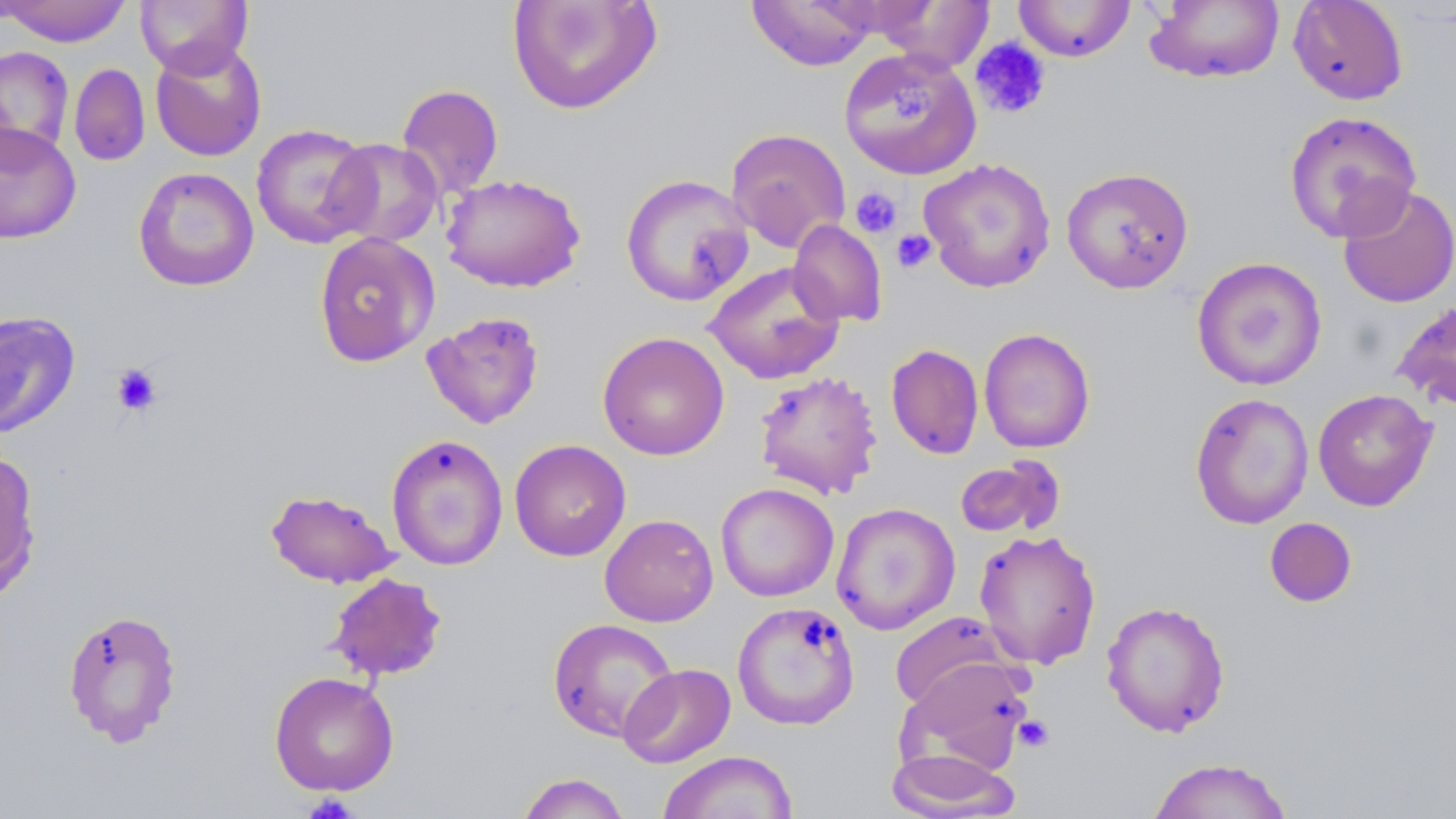

Approximate bounding boxes as [x1, y1, x2, y2] in pixels. Uninfected red blood cell locations: [2, 0, 133, 47], [135, 0, 252, 76], [507, 0, 661, 115], [747, 0, 880, 71], [875, 0, 994, 72], [1013, 0, 1135, 62], [1145, 0, 1285, 84], [1288, 0, 1409, 105], [150, 39, 267, 162], [0, 46, 74, 162], [839, 47, 982, 180], [69, 63, 150, 166], [397, 84, 504, 201], [1283, 110, 1423, 243], [0, 121, 82, 244], [250, 123, 377, 249], [725, 127, 851, 252], [324, 138, 444, 248], [918, 157, 1057, 293], [133, 166, 259, 292], [1061, 166, 1194, 293], [441, 173, 586, 293], [620, 173, 755, 307], [1337, 184, 1456, 309], [788, 219, 887, 327], [313, 232, 440, 368], [1191, 256, 1328, 391], [704, 260, 845, 385], [1391, 298, 1456, 411], [0, 311, 81, 439], [421, 311, 545, 429], [978, 327, 1095, 454], [597, 331, 729, 460], [885, 343, 984, 460], [753, 370, 884, 500], [1313, 388, 1437, 511], [1189, 392, 1314, 529], [386, 433, 509, 571], [509, 439, 631, 561], [0, 448, 42, 602], [954, 455, 1065, 541], [715, 483, 839, 602], [265, 488, 399, 589], [831, 502, 960, 635], [599, 514, 718, 627], [1264, 517, 1357, 608], [973, 528, 1101, 670], [325, 572, 448, 682], [1101, 600, 1230, 737], [732, 601, 860, 730], [61, 608, 183, 747], [890, 612, 1010, 713], [547, 618, 678, 741], [898, 658, 1034, 777], [619, 663, 735, 768], [269, 671, 399, 797], [886, 747, 1020, 819], [658, 750, 798, 819], [1147, 757, 1293, 818], [515, 772, 632, 819]. Platelet locations: [970, 38, 1051, 120], [893, 84, 940, 124], [849, 186, 903, 237], [892, 229, 937, 273], [111, 363, 163, 416], [1014, 715, 1055, 752], [302, 794, 359, 819]. Slide-level diagnosis: negative for blood parasites. Thin blood smear. Single field of view. May-Grünwald-Giemsa-stained preparation. Captured at 1000x magnification. Light microscopy. Image is 1456×819 pixels.